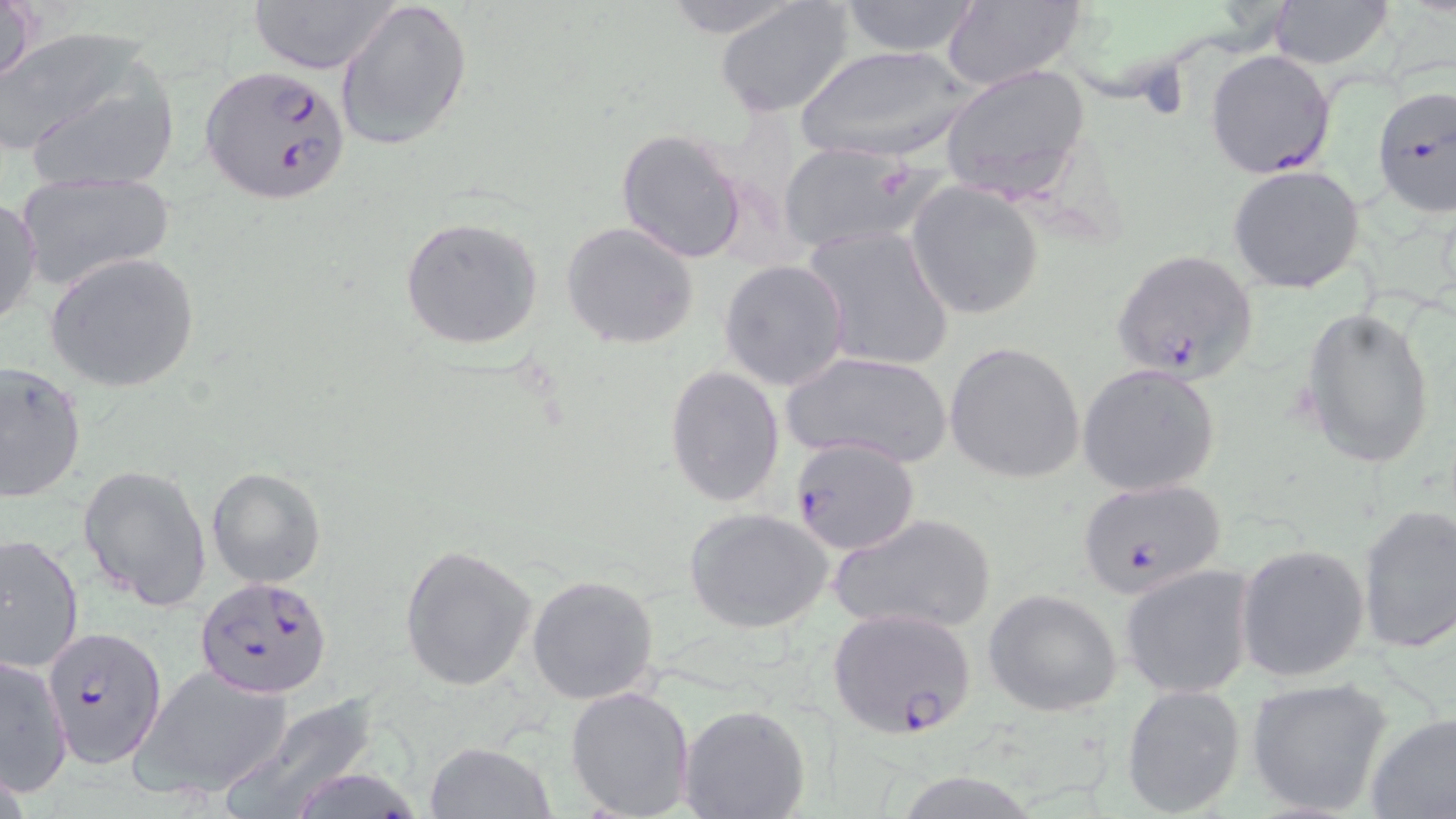

{
  "slide_level_diagnosis": "Plasmodium falciparum",
  "field_of_view": "single",
  "preparation": "thin blood smear",
  "stain": "May-Grünwald-Giemsa",
  "plasmodium_falciparum_infected_red_blood_cell_locations": "approximate bounding boxes as named x1/y1/x2/y2 corners in pixels: (x1=1205, y1=48, x2=1337, y2=180), (x1=200, y1=70, x2=350, y2=201), (x1=1372, y1=81, x2=1455, y2=217), (x1=1110, y1=248, x2=1260, y2=385), (x1=789, y1=436, x2=920, y2=558), (x1=1075, y1=478, x2=1228, y2=598), (x1=195, y1=576, x2=334, y2=699), (x1=826, y1=606, x2=979, y2=740), (x1=41, y1=627, x2=168, y2=768)",
  "uninfected_red_blood_cell_locations": "approximate bounding boxes as named x1/y1/x2/y2 corners in pixels: (x1=1, y1=0, x2=42, y2=92), (x1=334, y1=0, x2=474, y2=150), (x1=654, y1=0, x2=811, y2=40), (x1=716, y1=0, x2=859, y2=120), (x1=936, y1=0, x2=1087, y2=92), (x1=1268, y1=0, x2=1395, y2=69), (x1=245, y1=1, x2=402, y2=75), (x1=837, y1=1, x2=983, y2=57), (x1=7, y1=39, x2=181, y2=193), (x1=794, y1=45, x2=976, y2=163), (x1=940, y1=64, x2=1091, y2=201), (x1=613, y1=127, x2=749, y2=264), (x1=775, y1=141, x2=938, y2=256), (x1=1222, y1=169, x2=1361, y2=298), (x1=13, y1=171, x2=175, y2=292), (x1=906, y1=182, x2=1045, y2=321), (x1=0, y1=195, x2=42, y2=333), (x1=399, y1=216, x2=546, y2=351), (x1=561, y1=221, x2=700, y2=351), (x1=802, y1=224, x2=956, y2=374), (x1=45, y1=251, x2=200, y2=392), (x1=720, y1=259, x2=851, y2=391), (x1=1299, y1=305, x2=1437, y2=470), (x1=944, y1=342, x2=1085, y2=484), (x1=780, y1=348, x2=952, y2=469), (x1=0, y1=360, x2=87, y2=504), (x1=1077, y1=363, x2=1222, y2=496), (x1=664, y1=364, x2=784, y2=509), (x1=77, y1=462, x2=214, y2=612), (x1=207, y1=466, x2=326, y2=589), (x1=1355, y1=503, x2=1456, y2=654), (x1=684, y1=507, x2=832, y2=634), (x1=829, y1=511, x2=998, y2=635), (x1=2, y1=532, x2=83, y2=674), (x1=399, y1=543, x2=537, y2=692), (x1=1237, y1=543, x2=1371, y2=684), (x1=1119, y1=564, x2=1258, y2=699), (x1=526, y1=573, x2=661, y2=704), (x1=984, y1=588, x2=1124, y2=718), (x1=0, y1=655, x2=73, y2=795), (x1=129, y1=664, x2=295, y2=799), (x1=1244, y1=676, x2=1395, y2=817), (x1=565, y1=684, x2=696, y2=817), (x1=1121, y1=685, x2=1247, y2=817), (x1=222, y1=692, x2=384, y2=819), (x1=679, y1=705, x2=811, y2=819), (x1=1365, y1=710, x2=1456, y2=818), (x1=425, y1=741, x2=556, y2=819)",
  "image_size": "1456×819 pixels",
  "modality": "optical microscopy",
  "magnification": "1000x"
}